Report the malaria status of this cell.
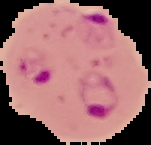
It is parasitized.

Summary:
  - Image type: segmented cell region with the area outside set to black
  - Image size: 151×145 pixels
  - Preparation: thin blood smear